Report the malaria status of this cell.
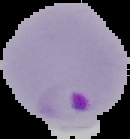

It is parasitized.

{
  "image_type": "segmented cell region with the area outside set to black",
  "preparation": "thin blood film",
  "image_size": "130×139 pixels"
}